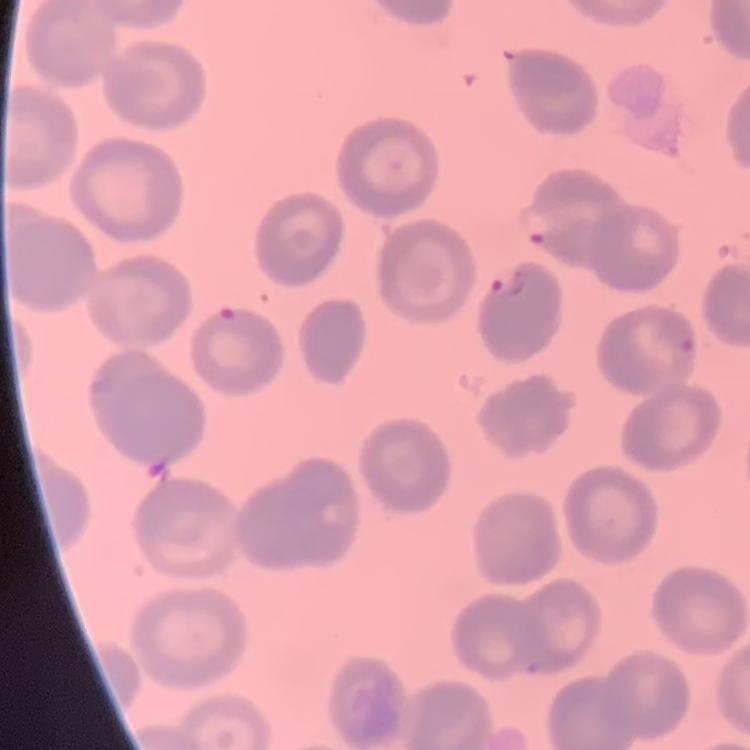

red blood cell morphology = no rouleaux formation
preparation = thin peripheral smear
image type = one tile cut from a larger photomicrograph
stain = Field's or Giemsa